Evaluate for malaria.
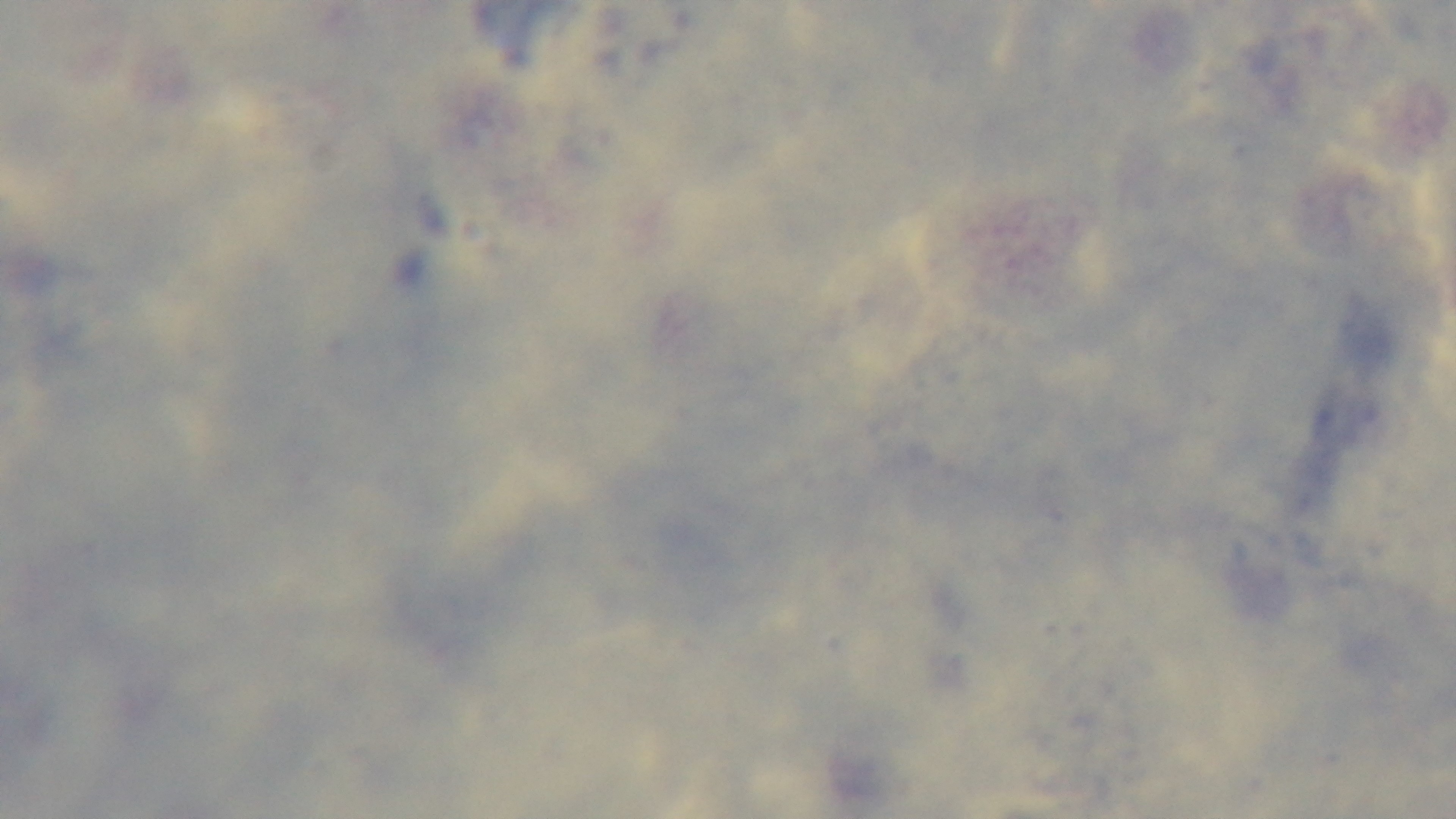

Uninfected.

Summary:
  - Capture: mounted 4K digital camera
  - Modality: light microscopy
  - Preparation: thick smear
  - Objective: 100x oil immersion
  - Stain: Giemsa
  - Field of view: one from the slide